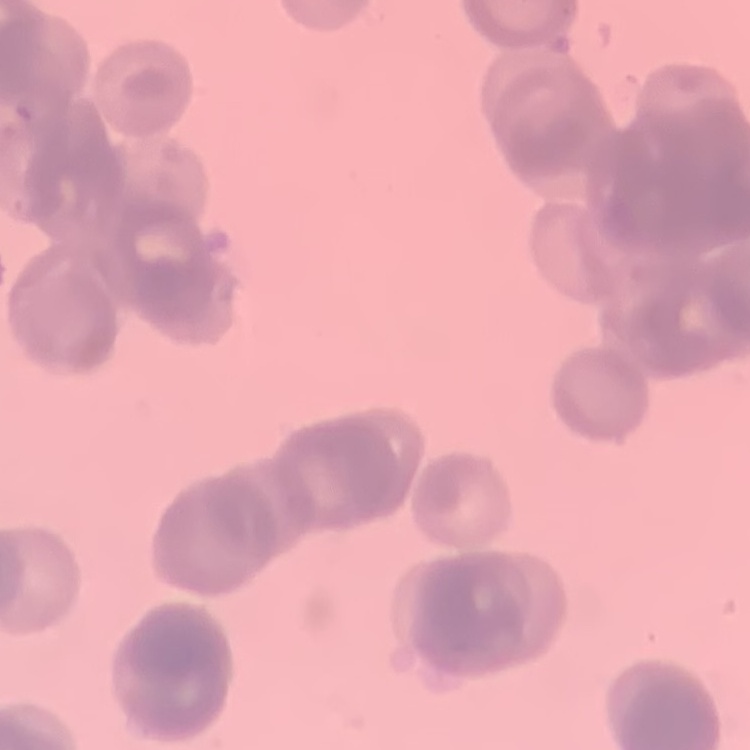
red blood cell morphology = rouleaux formation
stain = Field's or Giemsa
preparation = thin blood film
image type = one tile cut from a larger photomicrograph